Locate every uninfected red blood cell.
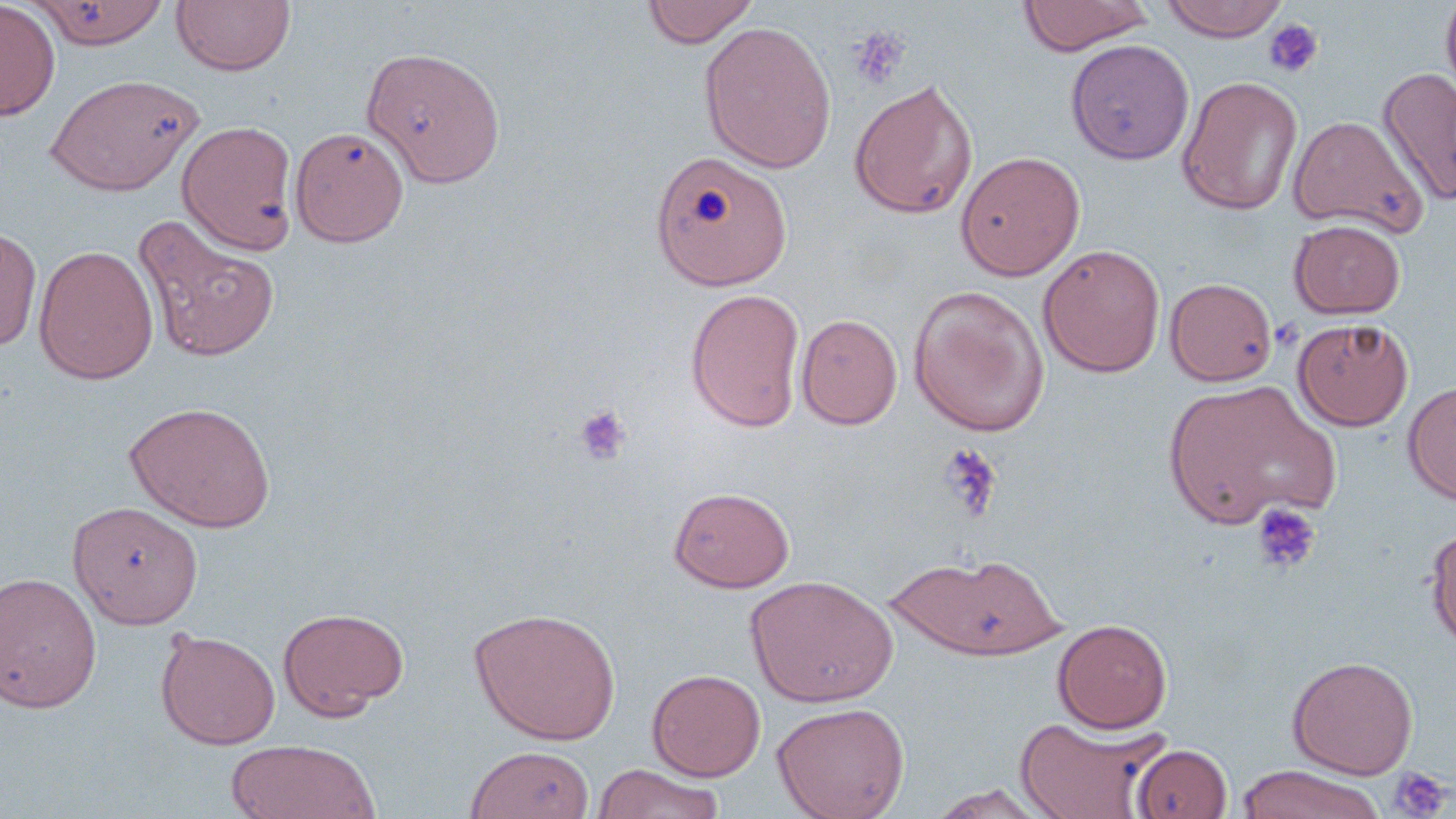
Approximate bounding boxes as (x1,y1)-(x2,y2) corner pairs in pixels.
Uninfected red blood cells: (171,0)-(296,76), (641,0)-(759,48), (1018,0)-(1153,55), (1160,0)-(1291,41), (1440,0)-(1456,108), (0,1)-(59,120), (28,1)-(168,48), (699,21)-(837,173), (1065,39)-(1194,165), (360,45)-(506,188), (1377,65)-(1456,208), (44,73)-(203,196), (1176,75)-(1303,215), (848,78)-(978,220), (1288,115)-(1425,235), (178,120)-(298,253), (290,126)-(410,246), (650,149)-(792,291), (955,150)-(1085,281), (133,216)-(281,362), (1289,219)-(1406,319), (0,225)-(42,352), (33,244)-(158,385), (1038,244)-(1165,377), (1165,277)-(1278,386), (909,284)-(1050,438), (685,287)-(806,433), (796,314)-(903,430), (1293,318)-(1414,431), (1162,378)-(1340,529), (1402,380)-(1456,504), (124,401)-(276,533), (669,486)-(795,593), (67,500)-(204,629), (1425,525)-(1456,651), (889,552)-(1065,661), (0,572)-(102,713), (746,575)-(898,707), (277,606)-(408,720), (469,607)-(622,745), (1052,618)-(1172,733), (155,628)-(280,750), (1287,656)-(1418,780), (647,668)-(765,781), (771,702)-(910,819), (1015,716)-(1168,818), (225,739)-(380,819), (1132,743)-(1233,818), (464,745)-(595,819), (593,764)-(724,819), (1236,764)-(1385,819), (926,784)-(1056,818).

Platelet locations: (1262,18)-(1323,79), (847,26)-(908,88), (572,405)-(631,466), (936,443)-(1003,524), (1249,502)-(1321,574), (1387,766)-(1451,818). Slide-level diagnosis: no evidence of blood parasites. May-Grünwald-Giemsa stain. Light microscopy. One field of a larger specimen. Captured at 1000x magnification. Image is 1456×819 pixels. Thin blood smear.